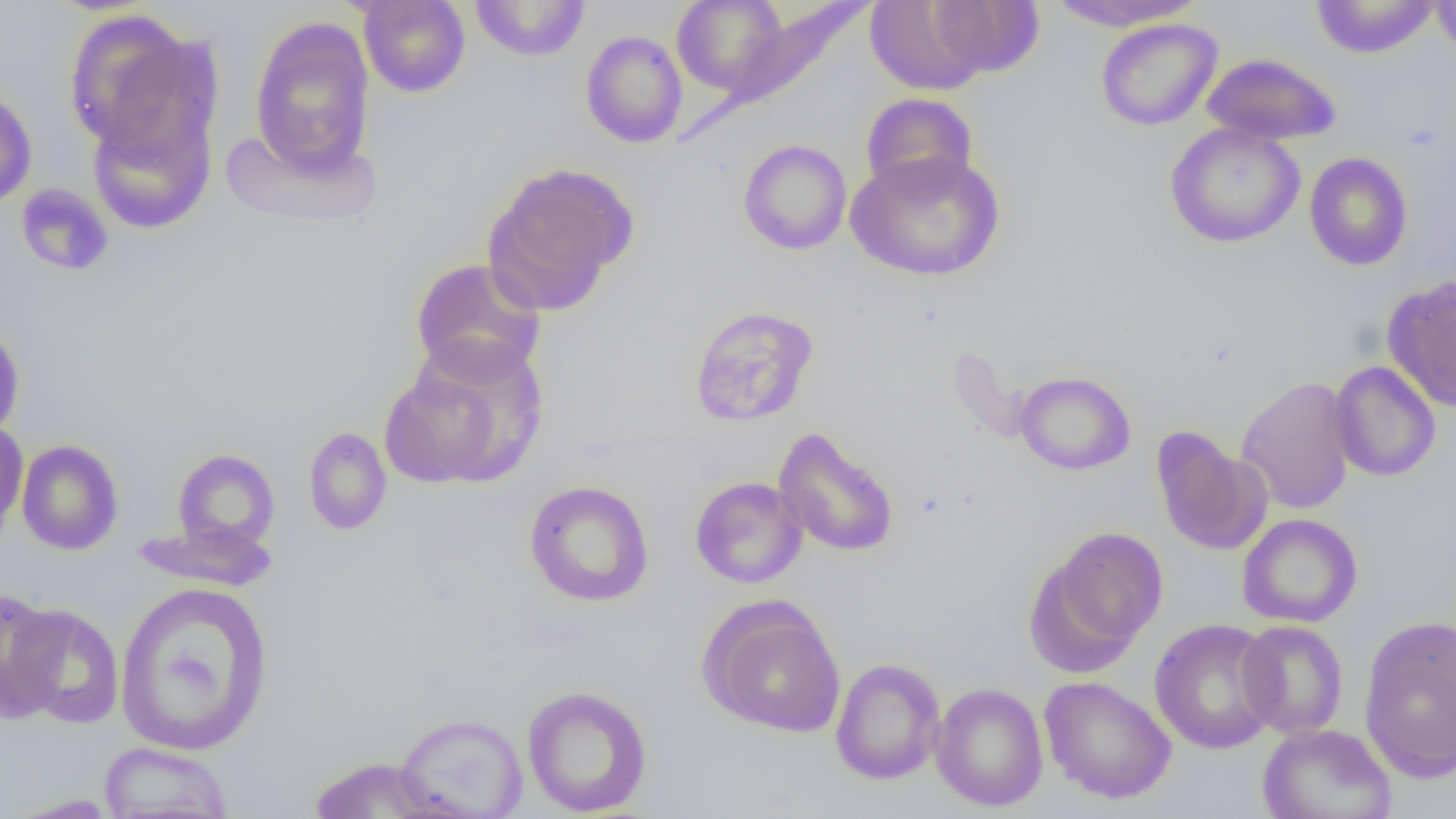
slide-level diagnosis = no evidence of blood parasites
field of view = single
magnification = 1000x
preparation = thin blood film
image size = 1456×819 pixels
modality = optical microscopy
uninfected red blood cell locations (subset) = approximate bounding boxes as (x1,y1)-(x2,y2) corner pairs in pixels: (357,0)-(470,98), (672,0)-(791,96), (920,0)-(1043,79), (1047,0)-(1206,32), (1310,0)-(1440,58), (1430,0)-(1456,58), (469,1)-(591,62), (865,1)-(994,95), (64,9)-(218,163), (248,16)-(377,177), (1096,18)-(1223,131), (580,30)-(688,148), (1201,52)-(1342,145), (0,86)-(37,209), (860,92)-(978,199), (87,98)-(217,235), (1165,122)-(1305,249), (738,138)-(852,255), (846,150)-(1005,282), (1304,152)-(1413,271), (483,161)-(638,312), (409,257)-(547,384), (1382,275)-(1456,411), (689,305)-(819,426), (0,318)-(25,443), (380,337)-(548,492), (1329,361)-(1441,482), (1014,371)-(1135,475), (1236,376)-(1357,515), (0,419)-(28,542), (303,427)-(392,536), (773,427)-(899,558), (1151,428)-(1272,556), (16,440)-(123,555), (172,449)-(280,553), (690,476)-(808,589), (524,480)-(655,607), (1237,513)-(1363,628), (132,518)-(279,592), (1035,525)-(1168,667), (114,582)-(275,755), (0,586)-(65,723), (702,599)-(847,738), (5,603)-(126,729), (1359,617)-(1456,781), (1149,618)-(1281,754), (1236,620)-(1349,739), (830,657)-(946,785), (1039,675)-(1177,804), (930,682)-(1049,812), (521,685)-(653,816), (394,712)-(529,818), (1257,723)-(1397,819), (98,741)-(234,819), (308,756)-(447,818), (5,793)-(125,818)